Assess this cell for malaria.
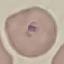
It is parasitized.

Thin blood smear. Giemsa-stained preparation. Automatically extracted cell patch, resized to 64 × 64 pixels. Acquired by smartphone through the microscope eyepiece.